State which parasite is depicted.
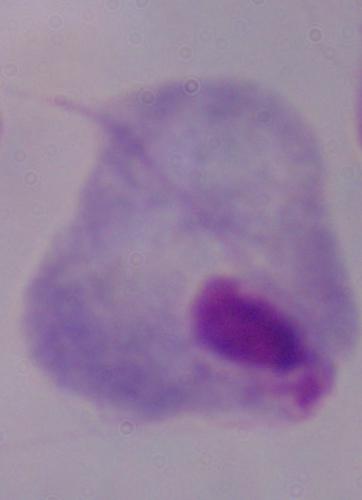
This is a trichomonad.

modality = micrograph
magnification = 1000x